Name the parasite shown.
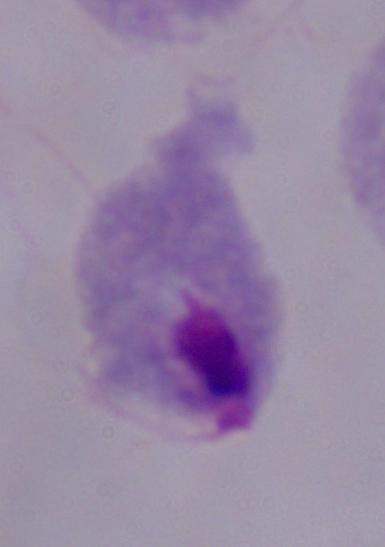

A trichomonad.

magnification: 1000x
modality: micrograph